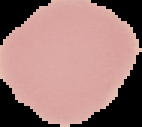 From a thin blood smear. The area outside the segmented cell region is set to black. Image is 142×127 pixels. Malaria status: uninfected.